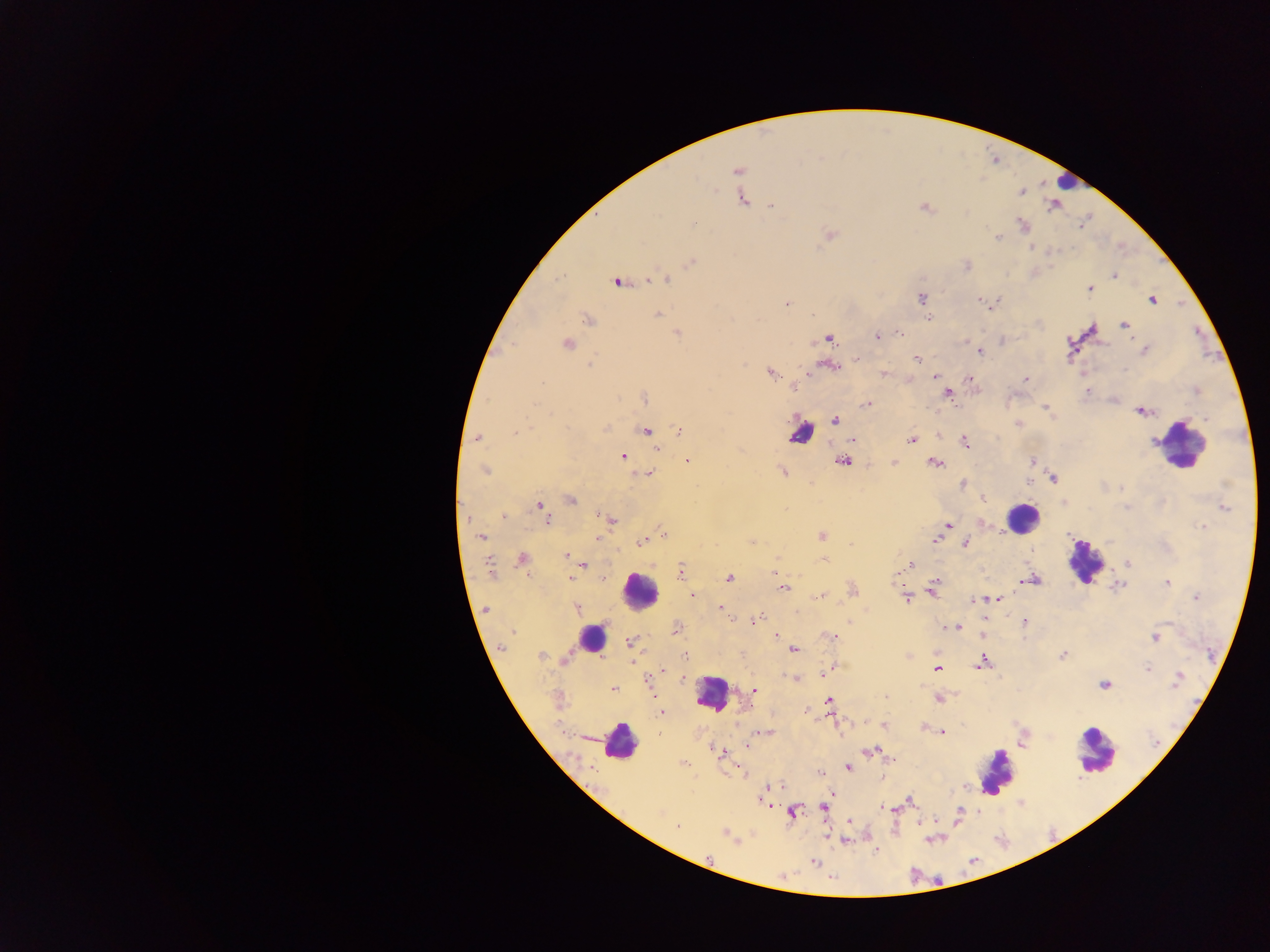 Approximate centers as {x, y} in pixels. Malaria parasite locations: {737, 171}, {1021, 193}, {742, 199}, {772, 205}, {925, 208}, {1023, 224}, {830, 234}, {998, 237}, {1032, 247}, {691, 262}, {967, 266}, {1114, 276}, {666, 279}, {616, 283}, {1090, 289}, {921, 298}, {979, 300}, {1152, 300}, {786, 304}, {993, 304}, {657, 315}, {929, 318}, {589, 319}, {1124, 325}, {900, 333}, {677, 334}, {877, 336}, {829, 338}, {566, 344}, {1145, 350}, {980, 351}, {916, 358}, {590, 366}, {831, 366}, {1124, 369}, {770, 373}, {883, 373}, {934, 376}, {969, 379}, {1026, 379}, {794, 388}, {1087, 391}, {949, 394}, {645, 398}, {865, 404}, {1045, 407}, {1140, 412}, {834, 420}, {605, 428}, {678, 430}, {646, 431}, {515, 433}, {477, 437}, {852, 439}, {911, 440}, {965, 442}, {656, 449}, {622, 456}, {687, 461}, {842, 461}, {1033, 461}, {894, 462}, {935, 463}, {484, 470}, {783, 472}, {648, 473}, {1052, 479}, {962, 484}, {1121, 488}, {982, 498}, {570, 500}, {1064, 502}, {539, 506}, {1225, 508}, {1128, 509}, {502, 516}, {610, 518}, {547, 519}, {948, 525}, {1201, 526}, {663, 533}, {822, 536}, {481, 537}, {597, 539}, {935, 540}, {643, 541}, {751, 542}, {965, 543}, {566, 556}, {522, 560}, {823, 560}, {1128, 564}, {584, 565}, {909, 565}, {490, 568}, {681, 570}, {775, 574}, {572, 578}, {729, 578}, {1034, 579}, {1026, 580}, {936, 582}, {1168, 583}, {783, 588}, {933, 589}, {853, 590}, {692, 595}, {817, 596}, {1195, 596}, {907, 598}, {997, 598}, {973, 601}, {577, 608}, {720, 608}, {485, 609}, {796, 611}, {755, 620}, {1025, 621}, {955, 627}, {676, 629}, {775, 636}, {983, 636}, {831, 637}, {1155, 637}, {629, 642}, {501, 647}, {793, 649}, {1063, 655}, {541, 656}, {684, 657}, {565, 658}, {632, 662}, {983, 662}, {1147, 668}, {937, 669}, {827, 671}, {663, 672}, {1178, 678}, {796, 679}, {1104, 684}, {613, 688}, {754, 691}, {885, 697}, {939, 699}, {828, 701}, {661, 713}, {883, 725}, {767, 732}, {942, 732}, {659, 734}, {746, 747}, {871, 752}, {720, 754}, {684, 764}, {848, 767}, {820, 773}, {762, 799}, {910, 800}, {884, 807}, {823, 808}, {661, 812}, {793, 812}, {920, 821}, {849, 822}, {677, 826}, {725, 834}, {845, 840}, {814, 862}. Leukocyte locations: {1065, 182}, {801, 433}, {1179, 445}, {1022, 517}, {1084, 561}, {639, 590}, {591, 639}, {711, 694}, {619, 742}, {1096, 752}, {996, 771}. Image is 1270×952 pixels. Sample from Ghana. Mobile-phone photograph taken through the microscope. Thick blood smear. One field of view.